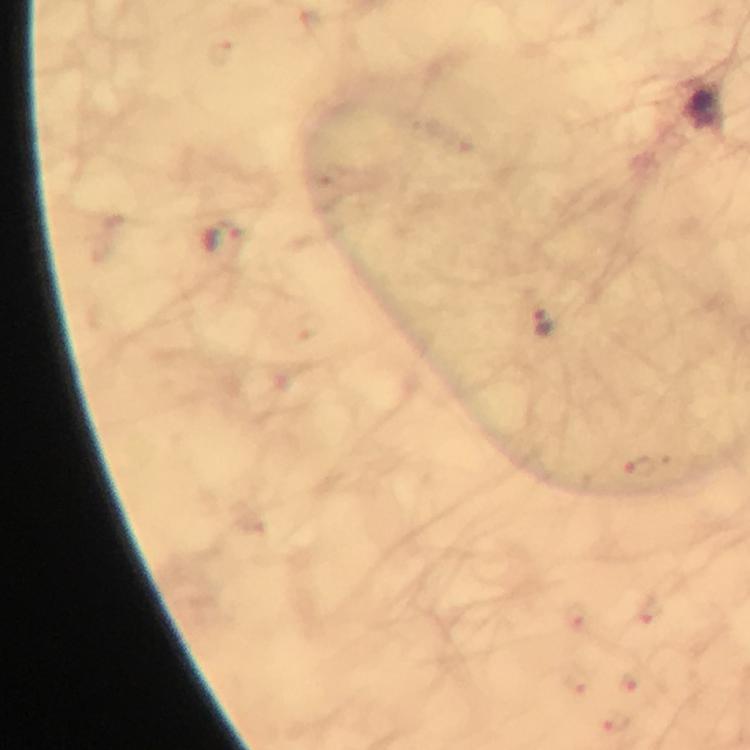
Approximate object centers, in pixels from the top-left corner.
Summary:
  - Malaria parasite locations: (x=223, y=241), (x=544, y=320), (x=640, y=468)
  - Cropped from: one field of view
  - Capture: smartphone camera through the microscope
  - Magnification: 100x
  - Preparation: thick blood smear
  - Context: from a diagnostic examination for malaria
  - Stain: Giemsa
  - Immersion oil: applied
  - Image size: 750×750 pixels